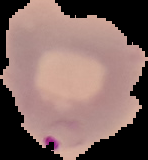

preparation: thin blood smear
image_type: segmented cell region with the area outside set to black
image_size: 148×160 pixels
result: Plasmodium parasites identified